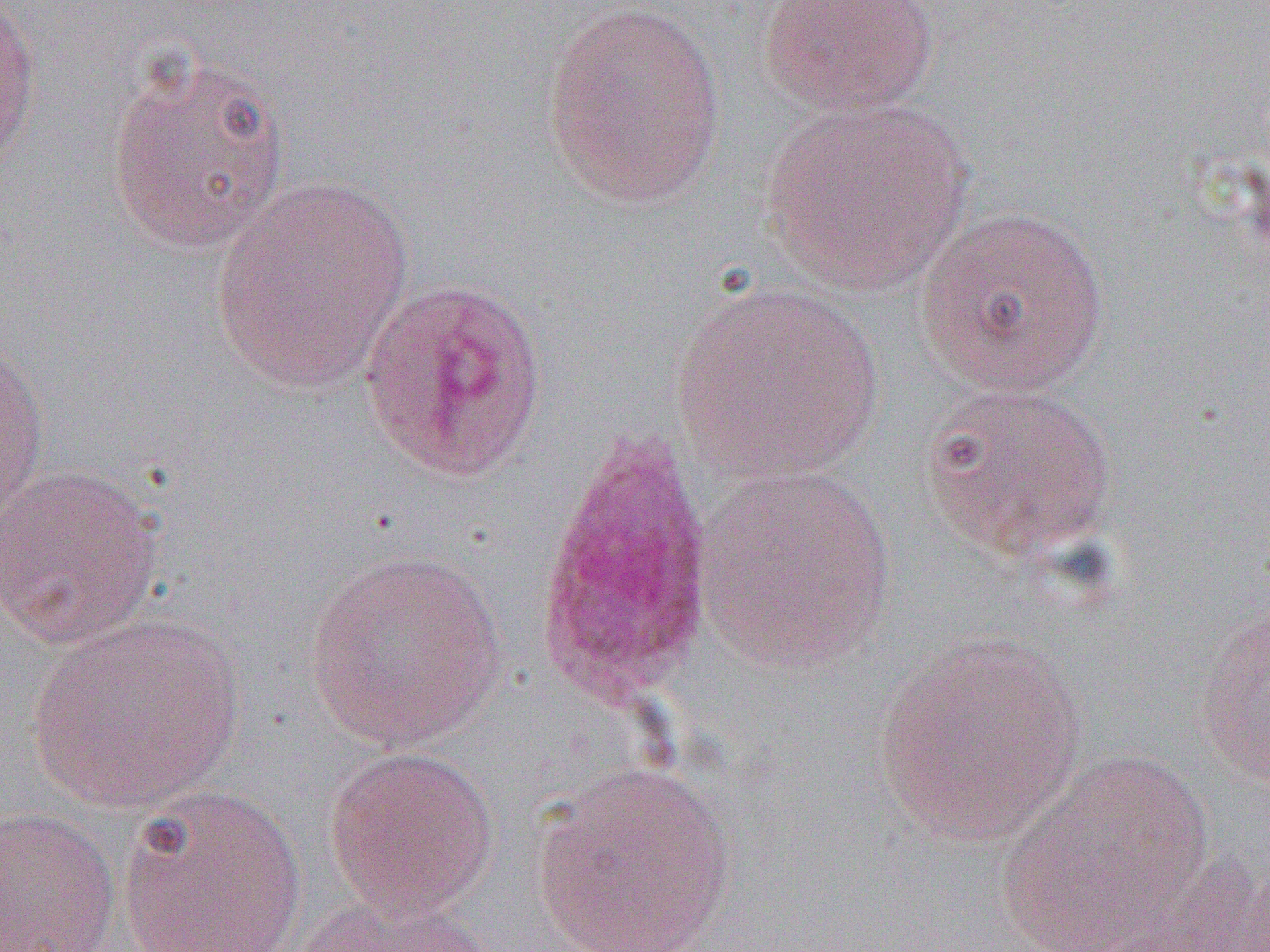 Approximate bounding boxes as [x1, y1, x2, y2] in pixels. Plasmodium ovale-infected red blood cell locations: [357, 276, 552, 483], [530, 433, 717, 707]. Uninfected red blood cell locations: [756, 0, 941, 117], [0, 1, 42, 177], [541, 1, 727, 208], [104, 48, 292, 255], [759, 96, 973, 295], [209, 178, 415, 393], [914, 206, 1110, 396], [671, 280, 883, 483], [0, 333, 50, 535], [919, 380, 1119, 564], [0, 463, 165, 649], [693, 463, 898, 670], [302, 548, 510, 750], [1193, 592, 1270, 795], [27, 612, 244, 813], [870, 632, 1086, 847], [323, 746, 500, 918], [998, 750, 1214, 949], [530, 761, 737, 951], [116, 782, 308, 952], [0, 807, 122, 952], [295, 889, 498, 952]. Slide-level diagnosis: Plasmodium ovale. Single field of view. Image is 1270×952 pixels. Thin blood film. Light microscopy. Captured at 1000x magnification.